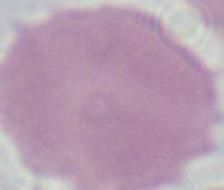

magnification = 1000x
identification = erythrocyte
modality = micrograph